Give the position of every Plasmodium parasite.
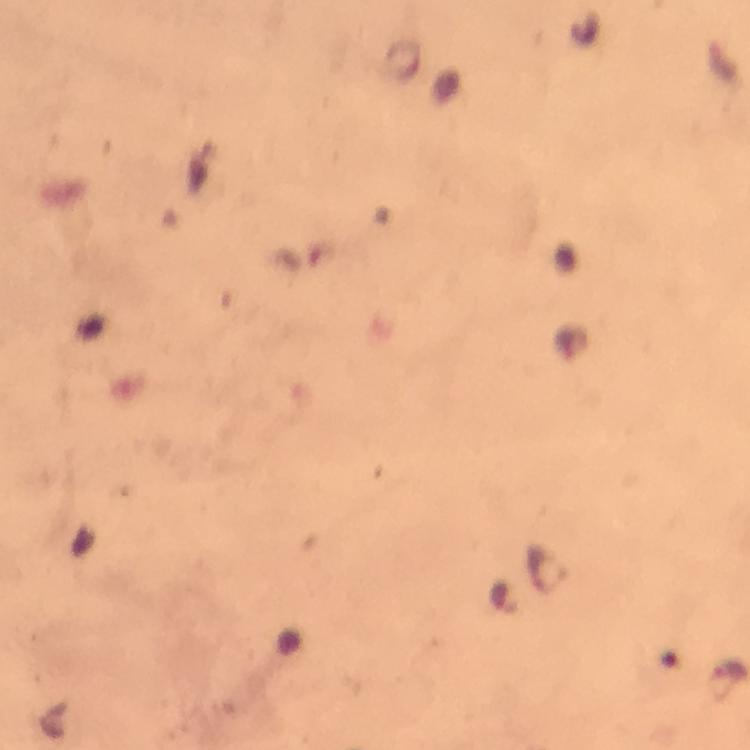
Approximate object centers, in pixels from the top-left corner.
Plasmodium parasites: (x=547, y=571), (x=504, y=598).

At 100x magnification. Giemsa-stained preparation. Immersion oil was used. Photographed with a smartphone mounted on the microscope. Image is 750×750 pixels. A crop from one field of view. Thick blood smear. From a malaria diagnostic workup.